Name the parasite shown.
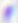

This is Toxoplasma gondii.

Summary:
  - Magnification: 400x
  - Modality: photomicrograph